Report the malaria status of this cell.
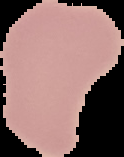

Uninfected.

Image is 124×157 pixels. From a thin blood film. Segmented cell region on a black background.